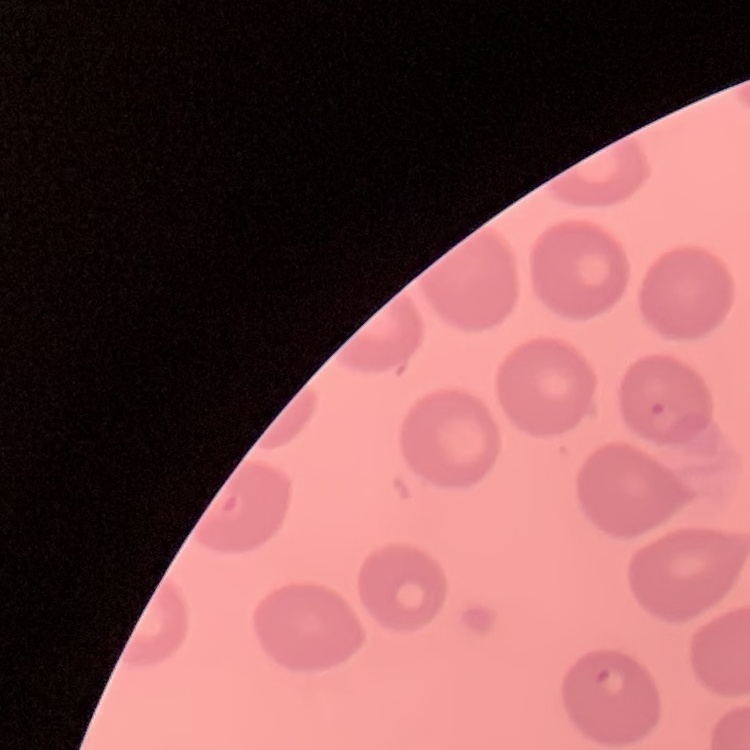

The red blood cells show no rouleaux formation. Field's or Giemsa stain. Thin peripheral smear. One tile cut from a larger photomicrograph.